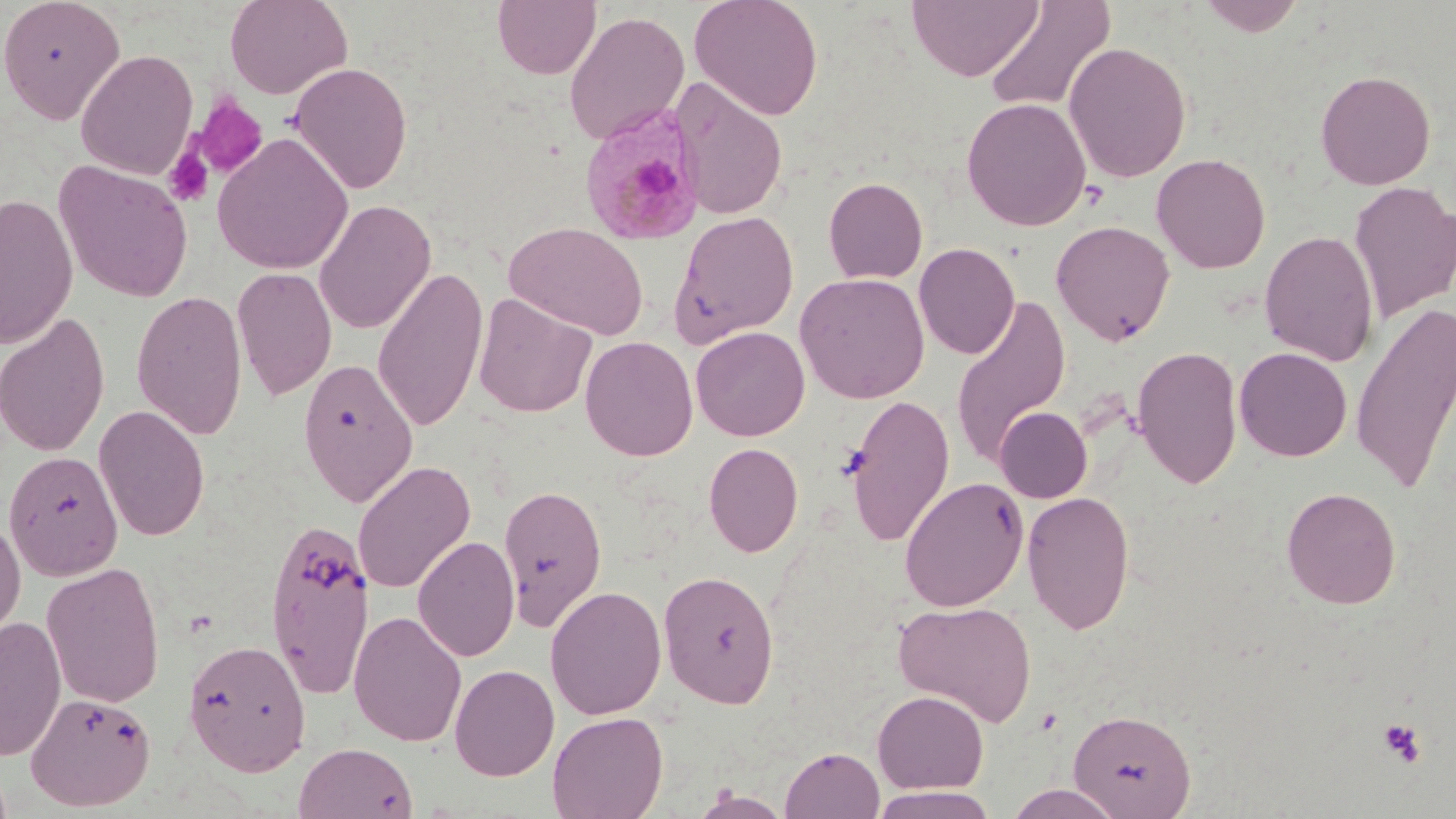

slide-level diagnosis = Plasmodium malariae
magnification = 1000x
field of view = single
Plasmodium malariae-infected red blood cell locations = approximate bounding boxes as [x1, y1, x2, y2] in pixels: [578, 106, 707, 247]
modality = light microscopy
image size = 1456×819 pixels
stain = May-Grünwald-Giemsa
platelet locations = approximate bounding boxes as [x1, y1, x2, y2] in pixels: [190, 95, 269, 180], [163, 146, 215, 208], [1378, 718, 1426, 768]
preparation = thin blood smear
uninfected red blood cell locations = approximate bounding boxes as [x1, y1, x2, y2] in pixels: [0, 0, 125, 124], [224, 0, 353, 99], [492, 0, 601, 80], [689, 0, 824, 120], [907, 0, 1044, 82], [983, 0, 1116, 116], [1196, 0, 1307, 36], [564, 11, 690, 146], [1063, 41, 1192, 183], [76, 49, 198, 180], [289, 62, 413, 194], [1315, 69, 1436, 190], [671, 77, 788, 221], [961, 97, 1091, 231], [213, 132, 353, 275], [1151, 153, 1271, 274], [54, 160, 194, 303], [823, 177, 928, 283], [1349, 181, 1456, 323], [1, 193, 78, 349], [314, 199, 436, 334], [668, 211, 800, 347], [1051, 220, 1175, 346], [504, 222, 649, 340], [1259, 229, 1379, 366], [913, 242, 1020, 359], [232, 266, 337, 400], [373, 266, 489, 433], [794, 273, 930, 403], [131, 289, 248, 440], [473, 293, 596, 418], [950, 294, 1071, 469], [1350, 301, 1456, 494], [0, 312, 110, 458], [691, 326, 810, 441], [580, 335, 699, 461], [1132, 345, 1243, 489], [1234, 346, 1352, 462], [297, 357, 418, 507], [843, 394, 956, 547], [94, 404, 210, 541], [994, 407, 1092, 502], [703, 442, 803, 557], [4, 450, 123, 581], [352, 459, 475, 595], [899, 476, 1029, 612], [498, 483, 608, 631], [1281, 486, 1401, 609], [1022, 490, 1135, 635], [0, 516, 26, 644], [264, 516, 375, 698], [413, 535, 520, 662], [41, 561, 166, 708], [658, 569, 780, 708], [545, 585, 667, 719], [893, 600, 1037, 727], [348, 610, 467, 747], [0, 615, 66, 761], [183, 638, 312, 776], [449, 663, 560, 781], [872, 689, 989, 793], [25, 692, 156, 811], [1068, 707, 1196, 818], [547, 710, 668, 819], [294, 741, 417, 819], [780, 746, 885, 819], [1004, 784, 1127, 818], [868, 787, 1001, 818], [690, 790, 794, 818]